Assess this cell for malaria.
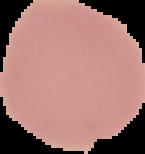

It is uninfected.

Cell region segmented out of the field of view; the surrounding area is masked to black. Image is 145×154 pixels. From a thin blood film.